Classify this cell by malaria status.
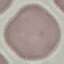
It is uninfected.

Thin blood smear. Photographed with a smartphone camera at the microscope eyepiece. Giemsa stain. Automatically extracted cell patch, resized to 64 × 64 pixels.